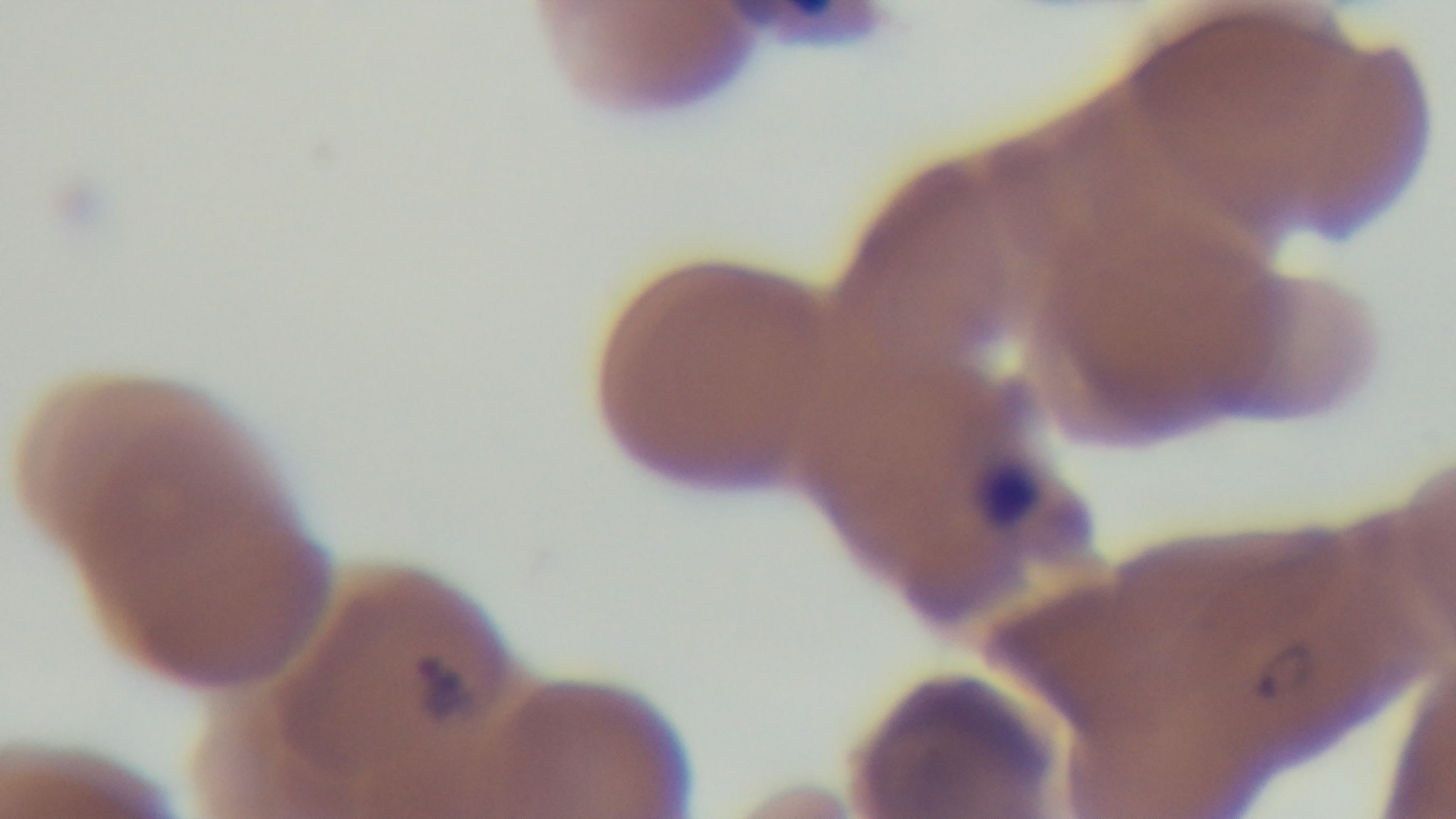
field of view = one from the slide
capture = mounted 4K digital camera
objective = 100x oil immersion
malaria status = infected
preparation = thin
modality = light microscopy
stain = Giemsa